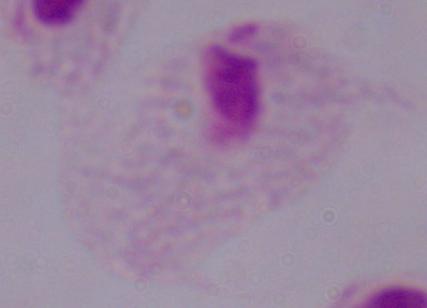 1000x magnification. A trichomonad is seen. Micrograph.